Identify the preparation type.
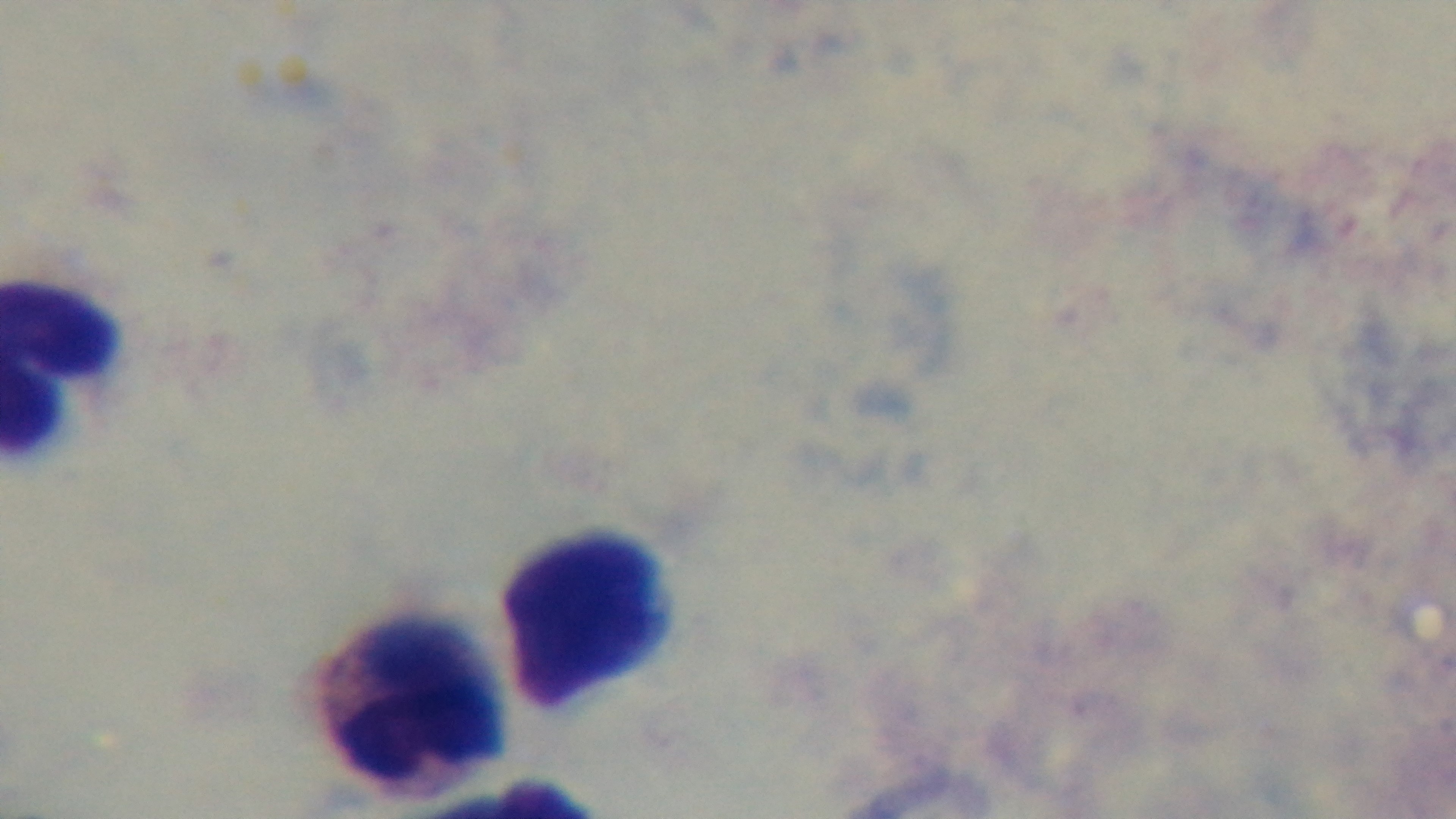
It is a thick blood film.

Summary:
  - Objective: 100x oil immersion
  - Field of view: one from the slide
  - Modality: light microscopy
  - Stain: Giemsa
  - Capture: mounted 4K digital camera
  - Malaria status: uninfected